Name the parasite shown.
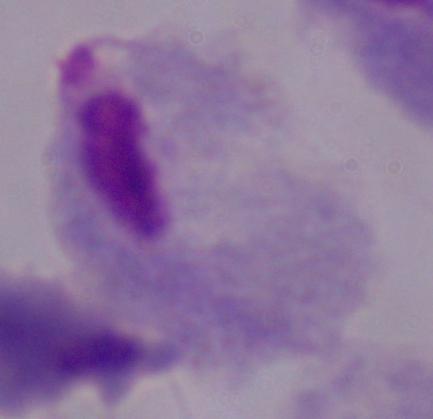
This is a trichomonad.

Micrograph. 1000x magnification.